Locate every malaria parasite.
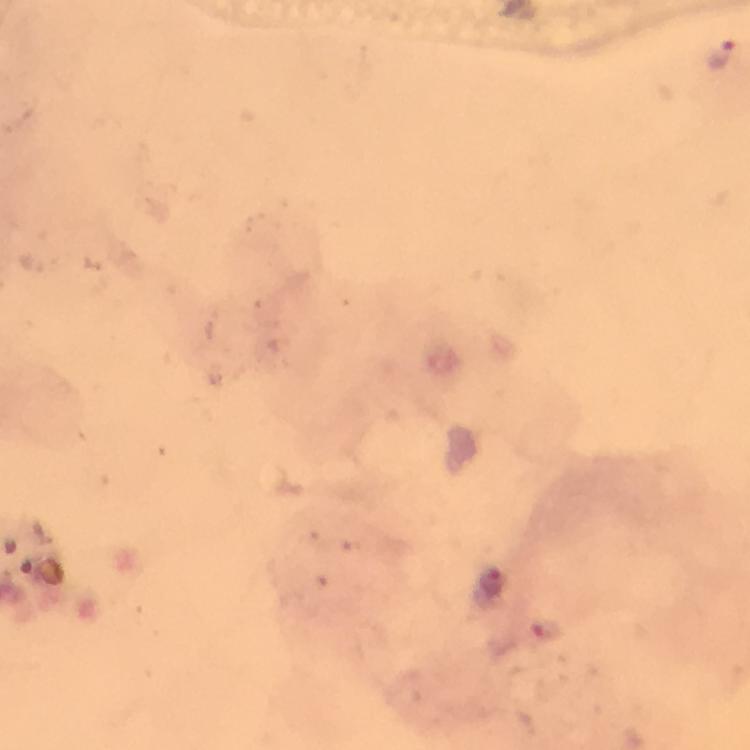
Approximate centers as (x, y) in pixels.
Malaria parasites: (723, 56), (490, 583), (547, 627).

Image is 750×750 pixels. 100x magnification. Immersion oil applied. Cropped region of a single field of view. Smartphone photograph taken through a microscope. From a malaria diagnostic workup. Giemsa-stained preparation. Thick blood film.